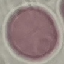
Result: no malaria parasites detected. Thin blood smear. Photographed with a smartphone camera at the microscope eyepiece. Automatically extracted cell patch, resized to 64 × 64 pixels. Giemsa stain.